Give the position of every malaria parasite.
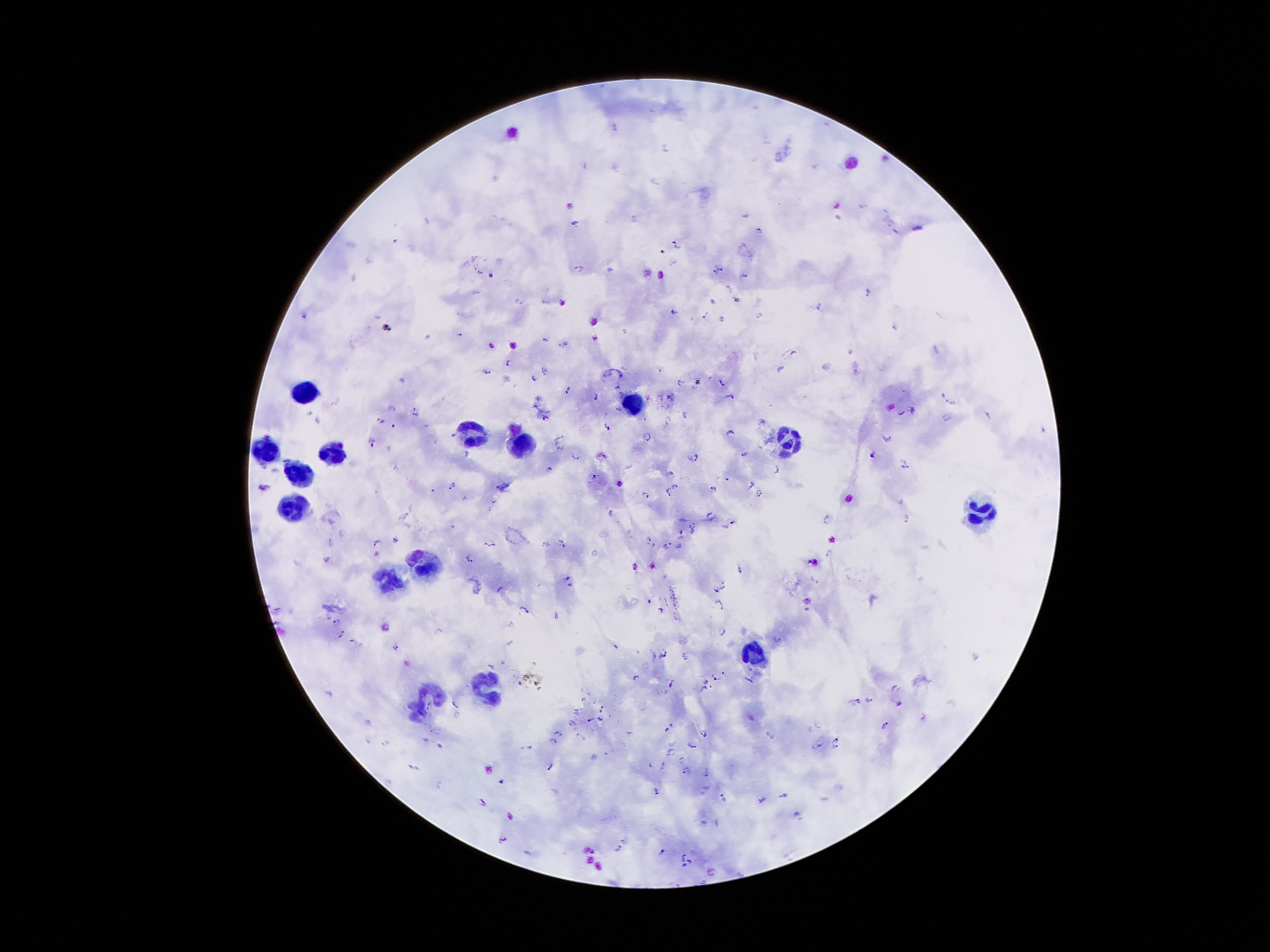

Approximate object centers, in pixels from the top-left corner.
Malaria parasites: (x=616, y=127), (x=667, y=146), (x=655, y=183), (x=862, y=205), (x=890, y=222), (x=573, y=224), (x=758, y=228), (x=674, y=241), (x=578, y=267), (x=721, y=268), (x=714, y=272), (x=491, y=275), (x=744, y=275), (x=729, y=288), (x=867, y=290), (x=819, y=307), (x=672, y=311), (x=706, y=315), (x=760, y=315), (x=721, y=319), (x=894, y=326), (x=459, y=333), (x=545, y=338), (x=492, y=346), (x=794, y=352), (x=507, y=362), (x=780, y=368), (x=543, y=371), (x=857, y=371), (x=487, y=372), (x=533, y=380), (x=678, y=381), (x=721, y=381), (x=616, y=386), (x=694, y=388), (x=567, y=389), (x=729, y=395), (x=594, y=397), (x=948, y=400), (x=392, y=408), (x=616, y=410), (x=914, y=410), (x=415, y=412), (x=900, y=413), (x=987, y=414), (x=685, y=415), (x=545, y=417), (x=379, y=419), (x=394, y=424), (x=607, y=426), (x=1044, y=429), (x=729, y=431), (x=562, y=437), (x=648, y=437), (x=887, y=440), (x=371, y=442), (x=559, y=449), (x=465, y=453), (x=745, y=453), (x=871, y=454), (x=575, y=457), (x=694, y=457), (x=904, y=465), (x=549, y=466), (x=671, y=472), (x=594, y=475), (x=750, y=483), (x=676, y=484), (x=451, y=485), (x=713, y=489), (x=432, y=490), (x=667, y=490), (x=758, y=493), (x=646, y=494), (x=494, y=501), (x=610, y=511), (x=906, y=516), (x=680, y=518), (x=732, y=521), (x=692, y=524), (x=682, y=531), (x=692, y=532), (x=649, y=537), (x=330, y=539), (x=395, y=539), (x=375, y=543), (x=489, y=543), (x=667, y=543), (x=563, y=544), (x=679, y=545), (x=829, y=553), (x=468, y=557), (x=326, y=559), (x=740, y=569), (x=567, y=577), (x=814, y=579), (x=722, y=582), (x=570, y=585), (x=499, y=587), (x=717, y=589), (x=648, y=600), (x=720, y=604), (x=525, y=607), (x=661, y=609), (x=805, y=609), (x=333, y=618), (x=511, y=622), (x=722, y=630), (x=342, y=632), (x=778, y=638), (x=354, y=641), (x=396, y=645), (x=615, y=646), (x=664, y=653), (x=489, y=666), (x=713, y=676), (x=635, y=677), (x=751, y=680), (x=704, y=681), (x=671, y=684), (x=702, y=689), (x=327, y=691), (x=868, y=698), (x=855, y=699), (x=897, y=702), (x=600, y=718), (x=588, y=719), (x=884, y=725), (x=666, y=729), (x=702, y=731), (x=556, y=733), (x=554, y=740), (x=384, y=742), (x=433, y=742), (x=836, y=742), (x=820, y=744), (x=692, y=745), (x=529, y=746), (x=668, y=751), (x=681, y=758), (x=662, y=762), (x=549, y=765), (x=415, y=766), (x=685, y=768), (x=500, y=780), (x=657, y=791), (x=782, y=794), (x=723, y=797), (x=761, y=798), (x=483, y=800), (x=798, y=813), (x=503, y=838), (x=623, y=840), (x=617, y=850), (x=662, y=851), (x=684, y=855), (x=689, y=861), (x=684, y=865).

Summary:
  - Leukocyte locations: (x=308, y=391), (x=634, y=397), (x=469, y=426), (x=790, y=442), (x=520, y=443), (x=265, y=448), (x=337, y=455), (x=299, y=472), (x=293, y=506), (x=978, y=513), (x=427, y=566), (x=386, y=579), (x=751, y=652), (x=483, y=685), (x=428, y=695)
  - Magnification: 100x
  - Image size: 1270×952 pixels
  - Preparation: thick blood smear
  - Capture: smartphone through the microscope eyepiece
  - Stain: Giemsa
  - Patient malaria status: positive for Plasmodium falciparum
  - Field of view: one from this slide